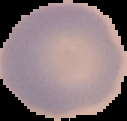

image_type: segmented cell region on a black background
malaria_status: uninfected
image_size: 127×121 pixels
preparation: thin blood smear